Find each parasitized red blood cell.
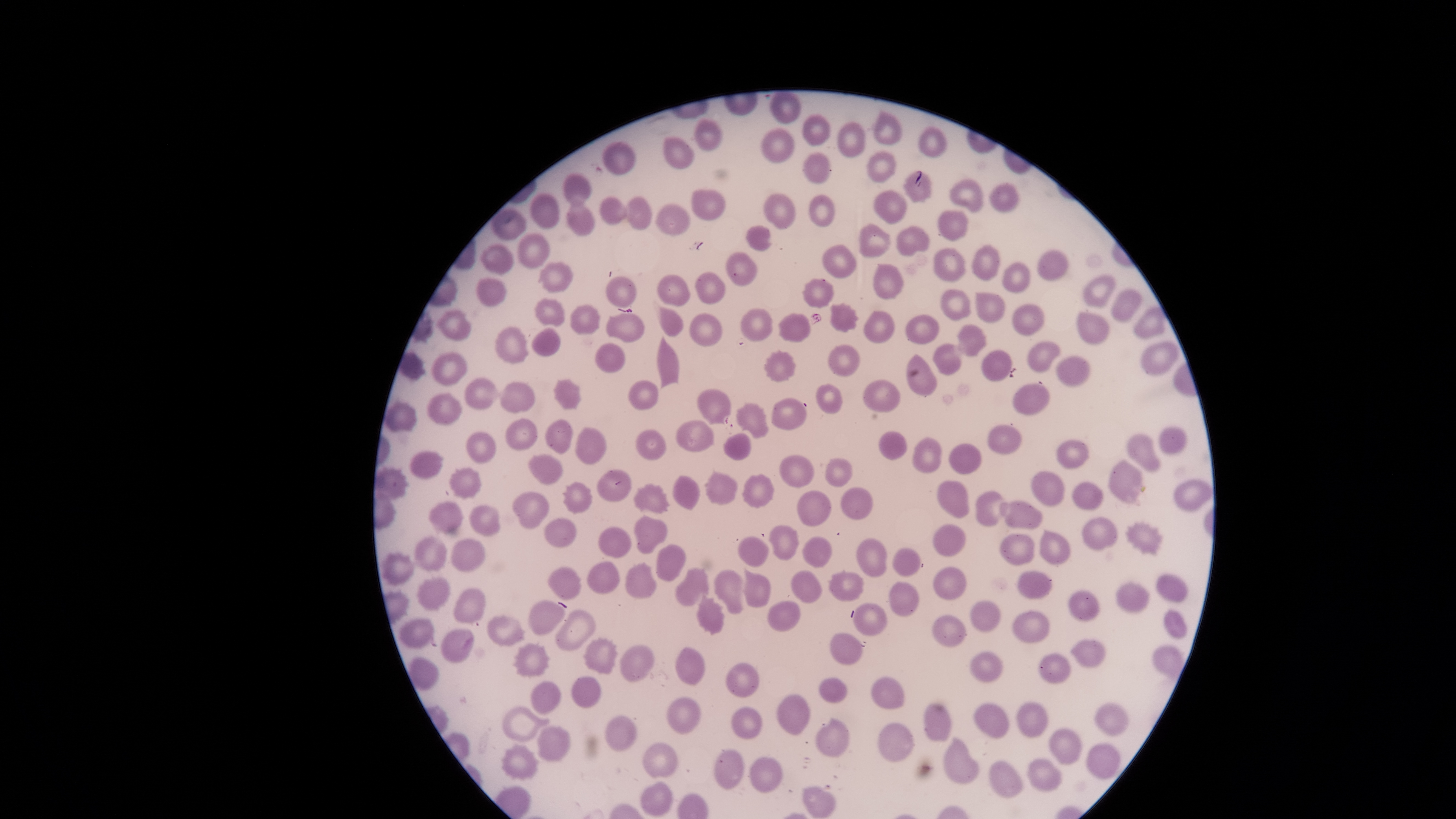
No parasitized red blood cells identified.

{
  "image_size": "1456×819 pixels",
  "uninfected_red_blood_cells": "approximate bounding boxes, in pixels from the top-left corner: (left=769, top=91, right=802, bottom=123), (left=873, top=109, right=902, bottom=145), (left=802, top=114, right=830, bottom=146), (left=694, top=117, right=723, bottom=150), (left=837, top=121, right=866, bottom=157), (left=919, top=126, right=947, bottom=159), (left=760, top=128, right=794, bottom=162), (left=664, top=137, right=693, bottom=169), (left=602, top=141, right=636, bottom=175), (left=802, top=152, right=831, bottom=185), (left=867, top=152, right=896, bottom=183), (left=903, top=171, right=931, bottom=202), (left=564, top=173, right=591, bottom=206), (left=950, top=178, right=983, bottom=213), (left=987, top=182, right=1018, bottom=213), (left=691, top=189, right=725, bottom=220), (left=873, top=190, right=907, bottom=225), (left=530, top=192, right=558, bottom=229), (left=763, top=193, right=795, bottom=229), (left=809, top=195, right=835, bottom=227), (left=599, top=196, right=625, bottom=225), (left=626, top=196, right=652, bottom=230), (left=566, top=200, right=594, bottom=237), (left=656, top=204, right=691, bottom=235), (left=492, top=209, right=526, bottom=240), (left=938, top=209, right=969, bottom=241), (left=859, top=223, right=890, bottom=258), (left=746, top=225, right=771, bottom=250), (left=895, top=226, right=929, bottom=256), (left=518, top=232, right=549, bottom=268), (left=480, top=244, right=513, bottom=274), (left=821, top=244, right=856, bottom=279), (left=971, top=244, right=1000, bottom=279), (left=933, top=247, right=966, bottom=282), (left=1038, top=249, right=1067, bottom=279), (left=726, top=252, right=758, bottom=286), (left=540, top=261, right=573, bottom=293), (left=1001, top=262, right=1029, bottom=292), (left=873, top=263, right=903, bottom=298), (left=695, top=272, right=725, bottom=303), (left=657, top=274, right=689, bottom=306), (left=1083, top=274, right=1114, bottom=308), (left=606, top=276, right=637, bottom=307), (left=476, top=278, right=507, bottom=307), (left=802, top=279, right=833, bottom=307), (left=940, top=289, right=970, bottom=320), (left=1112, top=289, right=1141, bottom=321), (left=976, top=293, right=1005, bottom=322), (left=535, top=298, right=564, bottom=326), (left=830, top=302, right=858, bottom=332), (left=570, top=304, right=600, bottom=334), (left=658, top=306, right=682, bottom=336), (left=741, top=308, right=772, bottom=342), (left=1133, top=308, right=1165, bottom=339), (left=863, top=310, right=894, bottom=344), (left=436, top=311, right=471, bottom=341), (left=1076, top=312, right=1108, bottom=344), (left=606, top=313, right=645, bottom=342), (left=689, top=313, right=722, bottom=346), (left=779, top=313, right=810, bottom=342), (left=904, top=314, right=939, bottom=343), (left=956, top=324, right=986, bottom=356), (left=496, top=326, right=527, bottom=363), (left=531, top=327, right=560, bottom=356), (left=657, top=336, right=678, bottom=389), (left=1027, top=342, right=1060, bottom=372), (left=1140, top=342, right=1179, bottom=375), (left=594, top=343, right=624, bottom=373), (left=932, top=343, right=961, bottom=375), (left=764, top=350, right=796, bottom=383), (left=981, top=350, right=1012, bottom=381), (left=431, top=352, right=467, bottom=384), (left=905, top=354, right=936, bottom=395), (left=1054, top=356, right=1089, bottom=385), (left=464, top=377, right=497, bottom=409), (left=552, top=379, right=582, bottom=410), (left=862, top=379, right=900, bottom=414), (left=628, top=380, right=657, bottom=411), (left=500, top=383, right=535, bottom=413), (left=1012, top=383, right=1050, bottom=415), (left=816, top=384, right=842, bottom=415), (left=696, top=388, right=731, bottom=424), (left=427, top=392, right=461, bottom=424), (left=771, top=398, right=806, bottom=429), (left=385, top=400, right=416, bottom=431), (left=736, top=403, right=768, bottom=438), (left=506, top=418, right=538, bottom=450), (left=545, top=418, right=574, bottom=454), (left=676, top=420, right=715, bottom=452), (left=989, top=425, right=1022, bottom=453), (left=575, top=428, right=607, bottom=464), (left=1159, top=428, right=1186, bottom=453), (left=636, top=429, right=665, bottom=459), (left=465, top=431, right=496, bottom=463), (left=723, top=432, right=751, bottom=460), (left=1126, top=434, right=1160, bottom=472), (left=912, top=436, right=941, bottom=473), (left=1055, top=440, right=1088, bottom=469), (left=410, top=451, right=442, bottom=478), (left=528, top=454, right=562, bottom=486), (left=779, top=456, right=814, bottom=487), (left=824, top=457, right=851, bottom=487), (left=1109, top=459, right=1142, bottom=503), (left=375, top=467, right=409, bottom=499), (left=448, top=467, right=481, bottom=500), (left=704, top=469, right=737, bottom=505), (left=597, top=470, right=630, bottom=502), (left=1031, top=470, right=1065, bottom=506), (left=742, top=474, right=773, bottom=509), (left=673, top=475, right=700, bottom=509), (left=936, top=479, right=969, bottom=518), (left=1174, top=480, right=1211, bottom=510), (left=561, top=481, right=592, bottom=513), (left=1073, top=483, right=1102, bottom=510), (left=633, top=484, right=669, bottom=514), (left=797, top=490, right=830, bottom=526), (left=974, top=490, right=1001, bottom=527), (left=512, top=491, right=549, bottom=528), (left=429, top=501, right=463, bottom=532), (left=998, top=501, right=1042, bottom=529), (left=468, top=505, right=500, bottom=537), (left=1082, top=516, right=1117, bottom=551), (left=634, top=517, right=666, bottom=554), (left=544, top=518, right=576, bottom=547), (left=1124, top=521, right=1165, bottom=555), (left=933, top=523, right=965, bottom=555), (left=769, top=526, right=799, bottom=560), (left=598, top=527, right=631, bottom=556), (left=1039, top=529, right=1070, bottom=565), (left=1000, top=534, right=1034, bottom=565), (left=414, top=535, right=447, bottom=571), (left=801, top=536, right=830, bottom=568), (left=738, top=537, right=769, bottom=568), (left=451, top=538, right=485, bottom=571), (left=856, top=538, right=886, bottom=576), (left=656, top=544, right=686, bottom=581), (left=893, top=547, right=920, bottom=577), (left=381, top=550, right=413, bottom=584), (left=587, top=560, right=619, bottom=594), (left=625, top=562, right=656, bottom=598), (left=548, top=567, right=580, bottom=599), (left=934, top=567, right=966, bottom=599), (left=676, top=568, right=708, bottom=606), (left=744, top=569, right=771, bottom=606), (left=828, top=569, right=863, bottom=601), (left=713, top=570, right=742, bottom=616), (left=1018, top=570, right=1051, bottom=598), (left=790, top=571, right=820, bottom=603), (left=1156, top=574, right=1187, bottom=601), (left=417, top=576, right=449, bottom=610), (left=889, top=582, right=919, bottom=617), (left=1116, top=584, right=1149, bottom=611), (left=454, top=588, right=485, bottom=624), (left=1070, top=590, right=1100, bottom=622), (left=695, top=593, right=724, bottom=635), (left=529, top=600, right=565, bottom=636), (left=767, top=601, right=799, bottom=630), (left=970, top=601, right=1001, bottom=631), (left=853, top=603, right=887, bottom=635), (left=555, top=610, right=595, bottom=651), (left=1164, top=610, right=1187, bottom=638), (left=1011, top=611, right=1050, bottom=642), (left=486, top=615, right=524, bottom=646), (left=932, top=615, right=965, bottom=647), (left=398, top=618, right=433, bottom=647), (left=441, top=629, right=474, bottom=663), (left=829, top=633, right=861, bottom=664), (left=583, top=638, right=618, bottom=673), (left=1069, top=639, right=1106, bottom=668), (left=512, top=642, right=551, bottom=677), (left=620, top=645, right=653, bottom=680), (left=1151, top=646, right=1183, bottom=677), (left=675, top=647, right=704, bottom=685), (left=969, top=651, right=1002, bottom=681), (left=1038, top=653, right=1070, bottom=683), (left=408, top=656, right=439, bottom=689), (left=725, top=662, right=758, bottom=697), (left=570, top=676, right=601, bottom=708), (left=870, top=676, right=904, bottom=708), (left=819, top=677, right=847, bottom=703), (left=530, top=681, right=560, bottom=714), (left=776, top=694, right=809, bottom=736), (left=666, top=697, right=701, bottom=734), (left=1016, top=701, right=1047, bottom=737), (left=1095, top=701, right=1128, bottom=734), (left=924, top=703, right=951, bottom=742), (left=974, top=703, right=1008, bottom=738), (left=503, top=707, right=550, bottom=741), (left=731, top=707, right=762, bottom=739), (left=606, top=716, right=636, bottom=751), (left=816, top=717, right=849, bottom=758), (left=877, top=722, right=914, bottom=761), (left=537, top=727, right=570, bottom=761), (left=1049, top=728, right=1082, bottom=765), (left=944, top=737, right=978, bottom=784), (left=642, top=742, right=677, bottom=779), (left=500, top=743, right=539, bottom=780), (left=1086, top=744, right=1120, bottom=778), (left=713, top=750, right=743, bottom=789), (left=749, top=756, right=783, bottom=791), (left=1027, top=758, right=1062, bottom=791), (left=988, top=761, right=1022, bottom=798), (left=640, top=781, right=672, bottom=816), (left=802, top=786, right=835, bottom=817)",
  "stain": "Giemsa",
  "visible_region": "circular",
  "preparation": "thin smear of blood",
  "field_of_view": "single",
  "capture": "smartphone photograph through the microscope eyepiece"
}